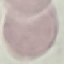

Malaria status: uninfected. Thin blood smear. Photographed with a smartphone camera at the microscope eyepiece. Cell patch, automatically extracted from a larger field of view and resized to 64 × 64 pixels. Giemsa stain.